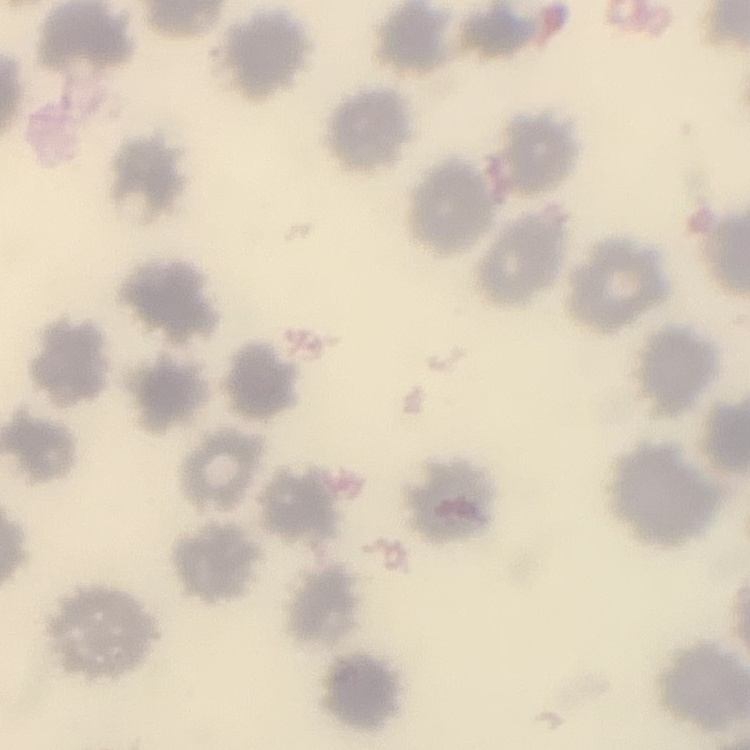

Summary:
  - Erythrocyte morphology: no rouleaux formation
  - Preparation: thin blood film
  - Stain: Field's or Giemsa
  - Image type: square crop of a larger photomicrograph